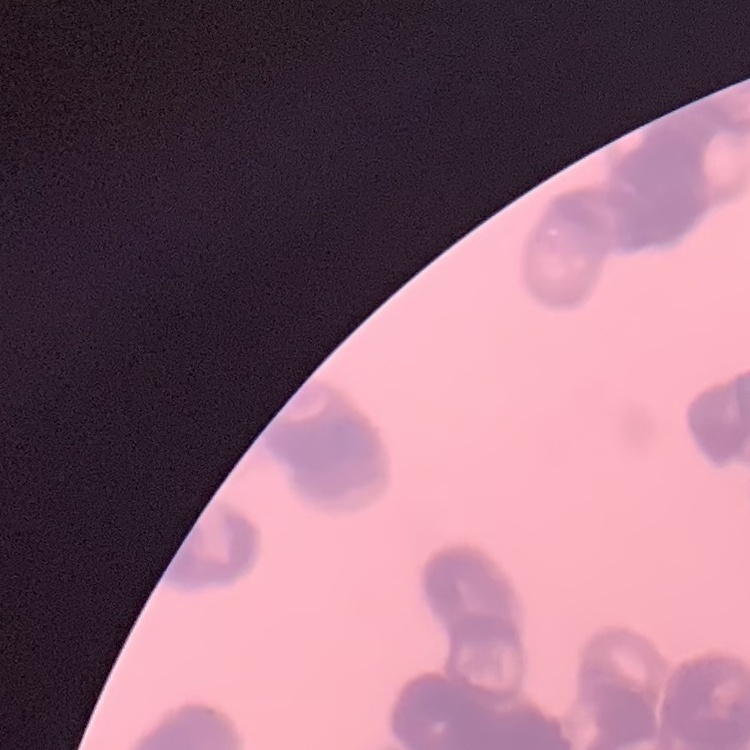
red_blood_cell_morphology: rouleaux formation
stain: Field's or Giemsa
image_type: square crop of a larger photomicrograph
preparation: thin blood smear